Name the blood parasite species.
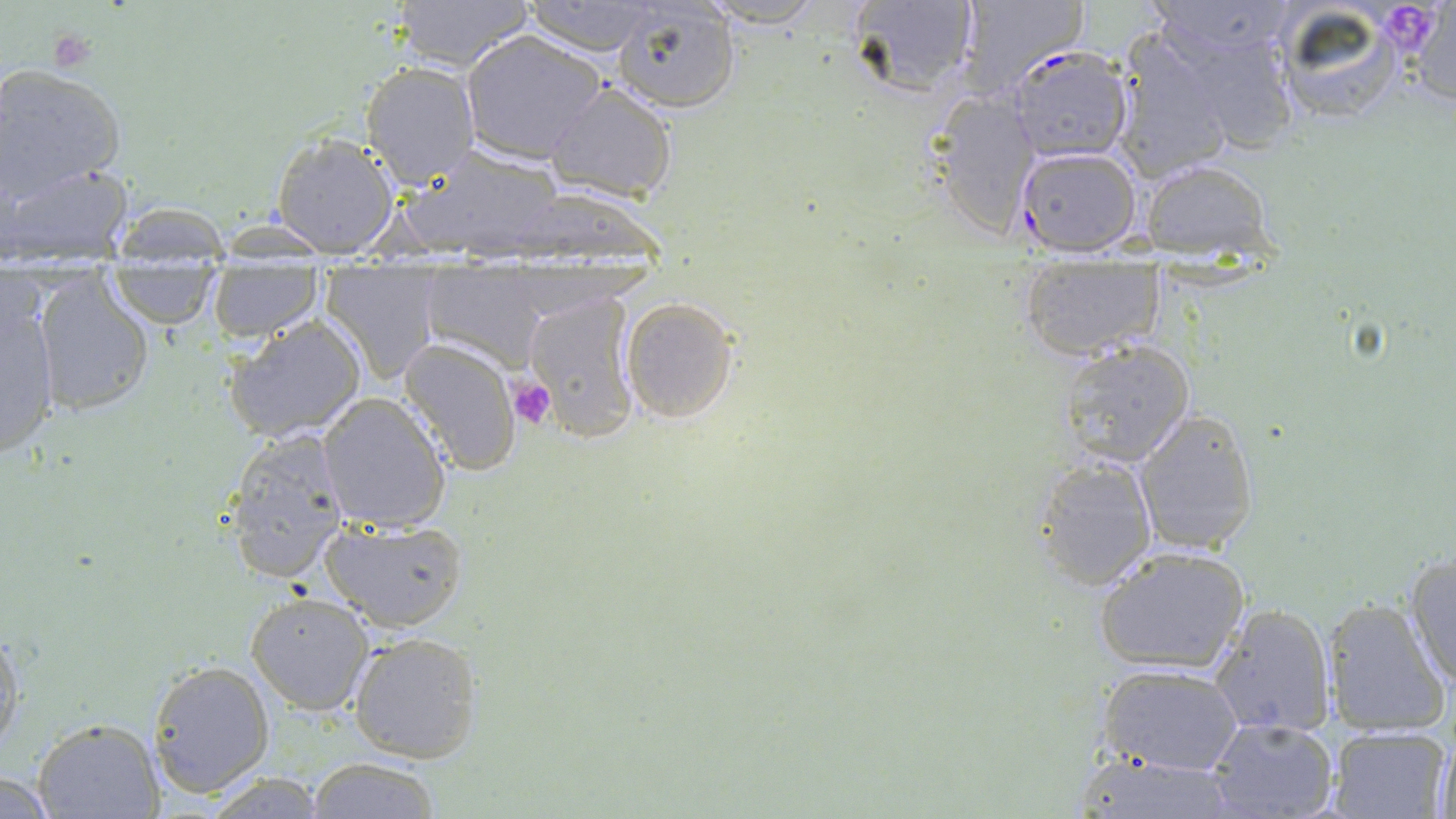

Plasmodium falciparum.

Summary:
  - Coordinate format: approximate bounding boxes as (x1, y1, x2, y2) in pixels
  - Uninfected red blood cell locations: (384, 0, 539, 71), (520, 0, 667, 54), (694, 0, 828, 28), (843, 0, 982, 101), (954, 0, 1084, 97), (1266, 0, 1411, 127), (1400, 0, 1456, 106), (613, 2, 741, 112), (1145, 13, 1302, 156), (461, 32, 606, 162), (1113, 36, 1237, 181), (361, 61, 482, 190), (0, 63, 127, 202), (545, 81, 678, 202), (926, 85, 1047, 234), (269, 130, 401, 257), (401, 143, 566, 259), (2, 158, 136, 264), (1139, 161, 1273, 262), (101, 210, 226, 331), (1019, 252, 1163, 361), (418, 263, 548, 367), (320, 267, 444, 382), (206, 268, 322, 341), (28, 273, 160, 417), (523, 290, 642, 439), (0, 292, 60, 461), (621, 296, 739, 423), (224, 315, 370, 443), (398, 337, 523, 478), (1054, 338, 1197, 469), (317, 392, 452, 533), (1131, 406, 1259, 557), (220, 426, 353, 586), (1036, 456, 1155, 587), (318, 518, 466, 633), (1093, 544, 1250, 675), (1401, 552, 1456, 696), (246, 591, 375, 714), (1322, 598, 1448, 736), (1211, 602, 1336, 737), (0, 627, 23, 757), (347, 632, 482, 765), (146, 659, 274, 797), (1096, 662, 1245, 776), (1205, 716, 1339, 819), (30, 717, 166, 819), (1326, 726, 1451, 818), (1431, 736, 1456, 819), (1067, 753, 1245, 818), (306, 757, 442, 817), (0, 769, 59, 819), (202, 772, 332, 817)
  - Platelet locations: (47, 29, 100, 77), (510, 377, 557, 430)
  - Plasmodium falciparum-infected red blood cell locations: (1005, 46, 1134, 163), (1013, 146, 1142, 257)
  - Modality: light microscopy
  - Stain: May-Grünwald-Giemsa
  - Preparation: thin blood smear
  - Field of view: one of a larger specimen
  - Magnification: 1000x
  - Image size: 1456×819 pixels